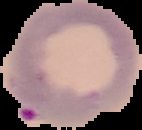
Malaria status: parasitized. Image is 142×130 pixels. Segmented cell region on a black background. From a thin blood film.